Describe the morphology of the erythrocytes.
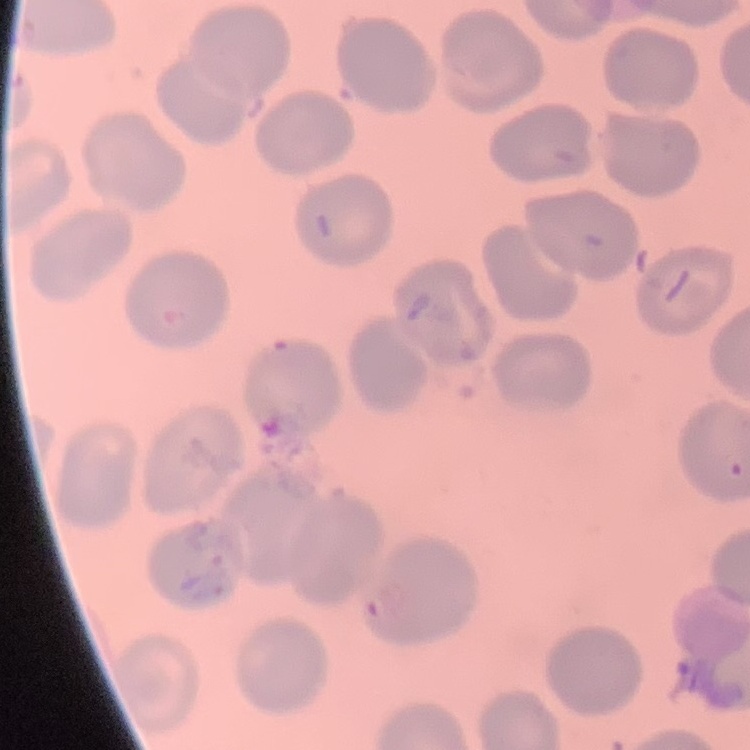

They show no rouleaux formation.

image_type: square crop of a larger photomicrograph
preparation: thin blood film
stain: Field's or Giemsa